Locate every Plasmodium parasite.
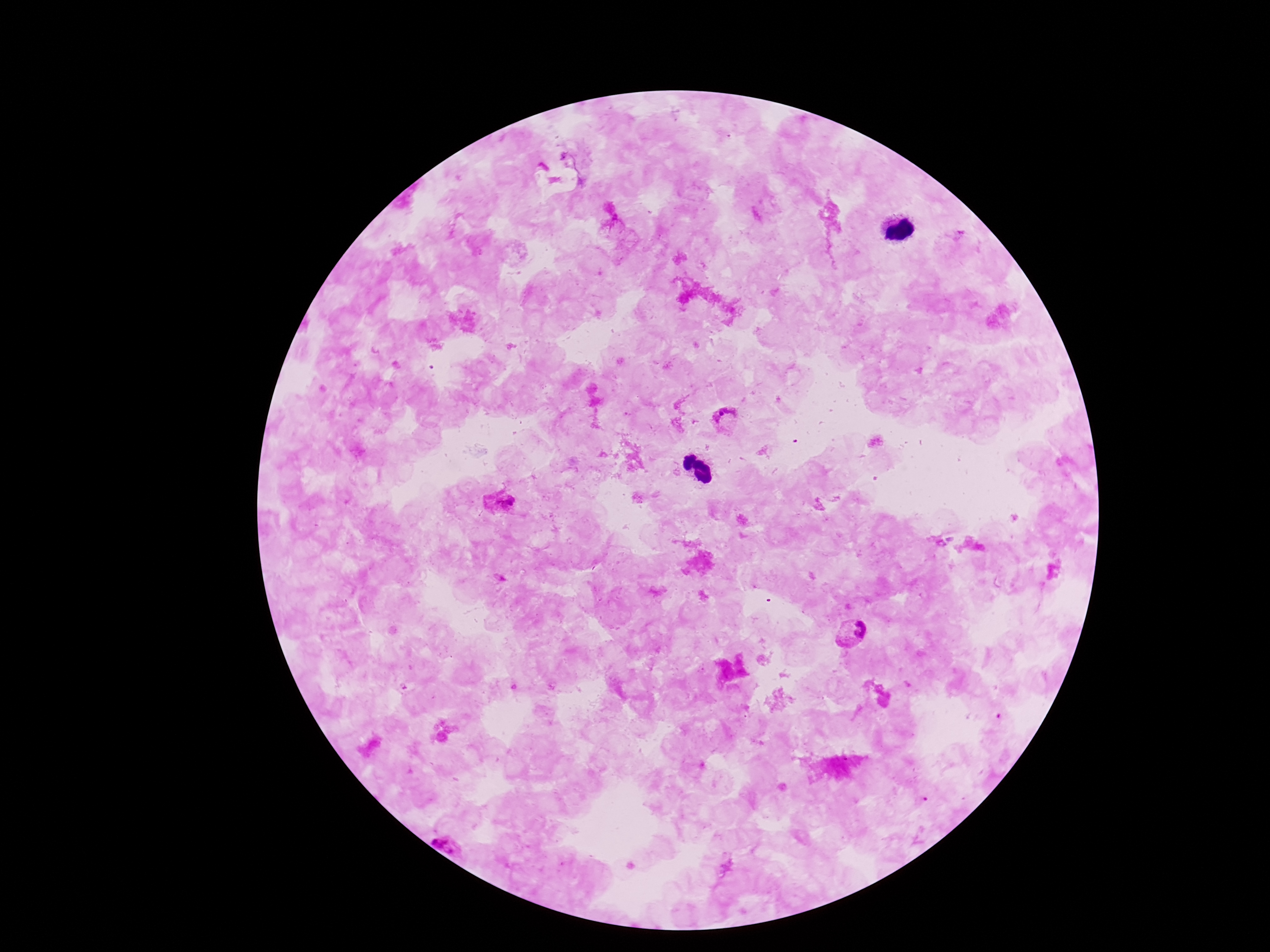

Approximate centers as (x, y) in pixels.
Plasmodium parasites: (726, 420), (500, 503), (853, 634), (453, 838).

Image is 1270×952 pixels. Thick blood smear. Single field of view. Smartphone photograph taken through the microscope eyepiece. Patient malaria status: infected. 100x magnification. Giemsa-stained preparation.